Report the malaria status of this cell.
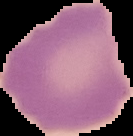

Uninfected.

image type = segmented cell region with the area outside set to black
image size = 133×136 pixels
preparation = thin blood film